Name the parasite shown.
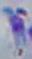

Toxoplasma gondii.

modality = photomicrograph
magnification = 1000x